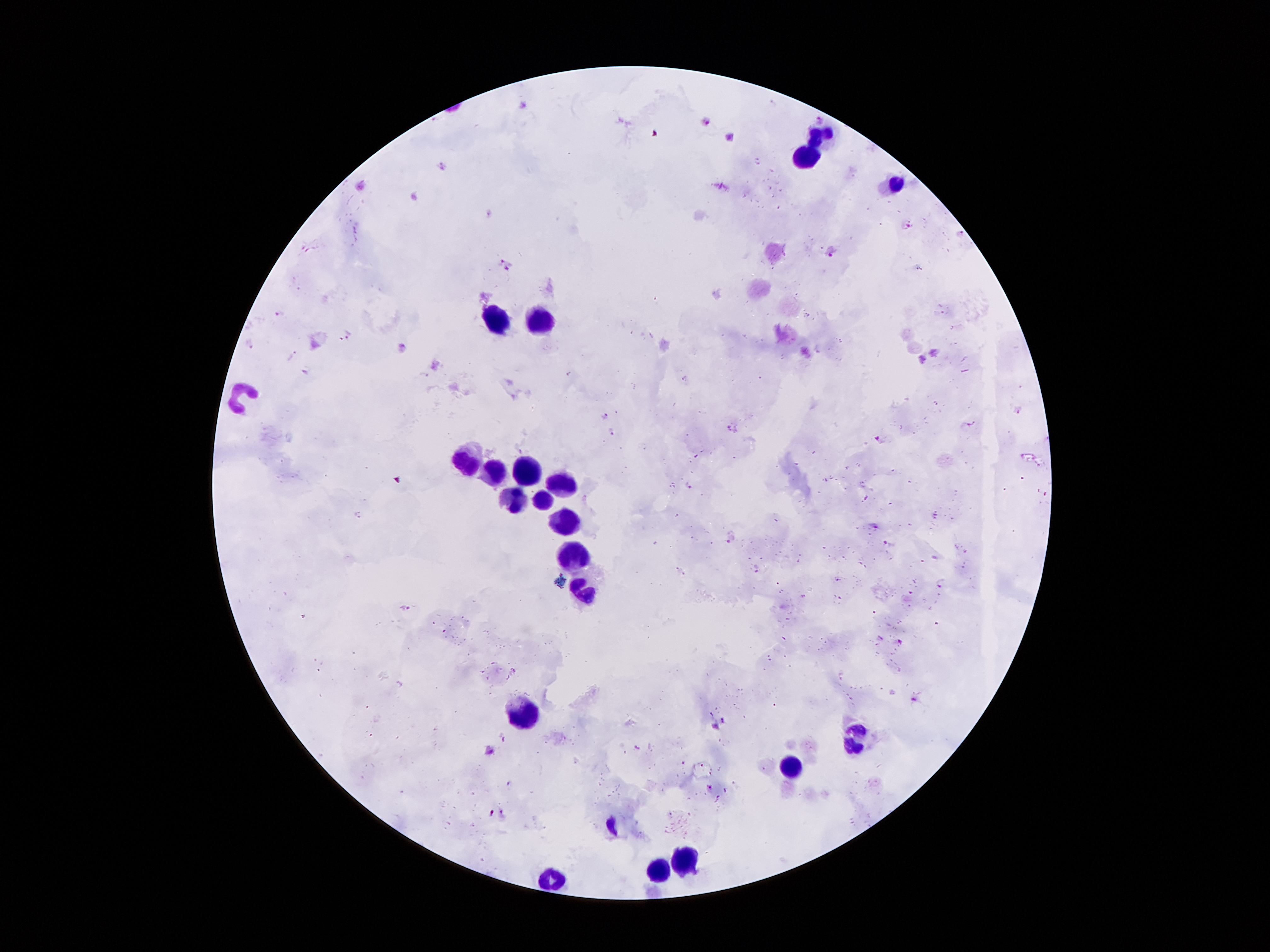

coordinate format = approximate centers as (x, y) in pixels
leukocyte locations = (817, 135), (807, 156), (895, 188), (498, 321), (539, 323), (243, 396), (468, 466), (495, 472), (527, 472), (570, 488), (514, 501), (544, 502), (568, 523), (572, 554), (585, 593), (523, 716), (857, 738), (792, 769), (687, 858), (658, 872), (555, 881)
malaria parasite locations = (821, 119), (704, 122), (442, 167), (906, 226), (831, 252), (508, 265), (281, 314), (605, 417), (612, 432), (879, 440), (729, 538), (405, 607), (901, 641), (913, 700), (722, 721), (509, 784), (710, 789), (490, 813), (500, 813)
patient malaria status = positive for Plasmodium falciparum
magnification = 100x
stain = Giemsa
capture = smartphone camera through the microscope eyepiece
preparation = thick blood film
image size = 1270×952 pixels
field of view = single